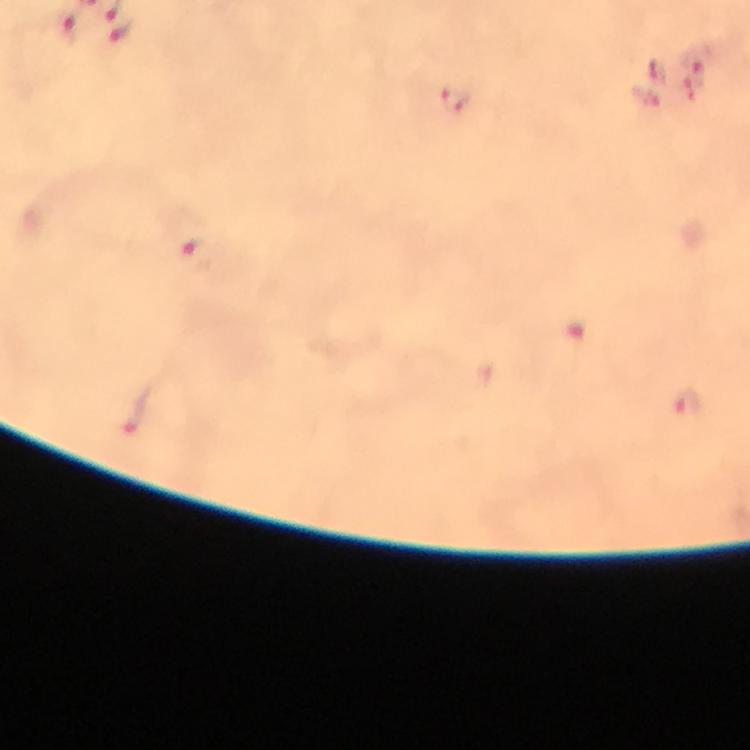
Approximate object centers, in pixels from the top-left corner. Plasmodium parasite locations: (x=68, y=24), (x=121, y=29), (x=697, y=55), (x=656, y=72), (x=457, y=98), (x=197, y=255), (x=687, y=403). Thick blood smear. At 100x magnification. From a diagnostic examination for malaria. Immersion oil was used. Image is 750×750 pixels. Giemsa-stained preparation. A crop from one field of view. Photographed through the microscope with a smartphone camera.